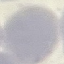
malaria status = uninfected
stain = Giemsa
preparation = thin smear
capture = smartphone through the microscope eyepiece
image type = cell patch, automatically extracted from a larger field of view and resized to 64 × 64 pixels